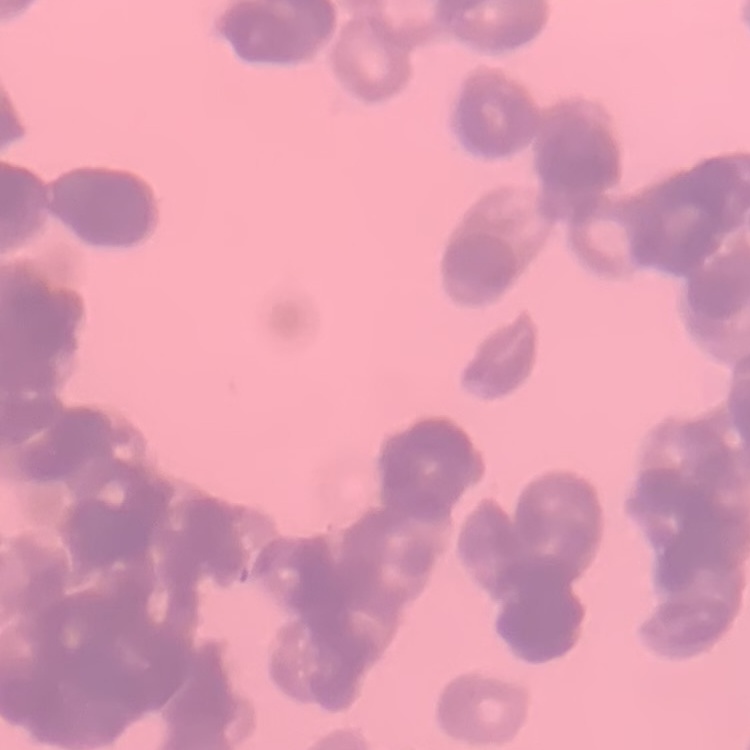 The red blood cells exhibit rouleaux formation. Field's or Giemsa stain. One tile cut from a larger photomicrograph. Thin blood film.